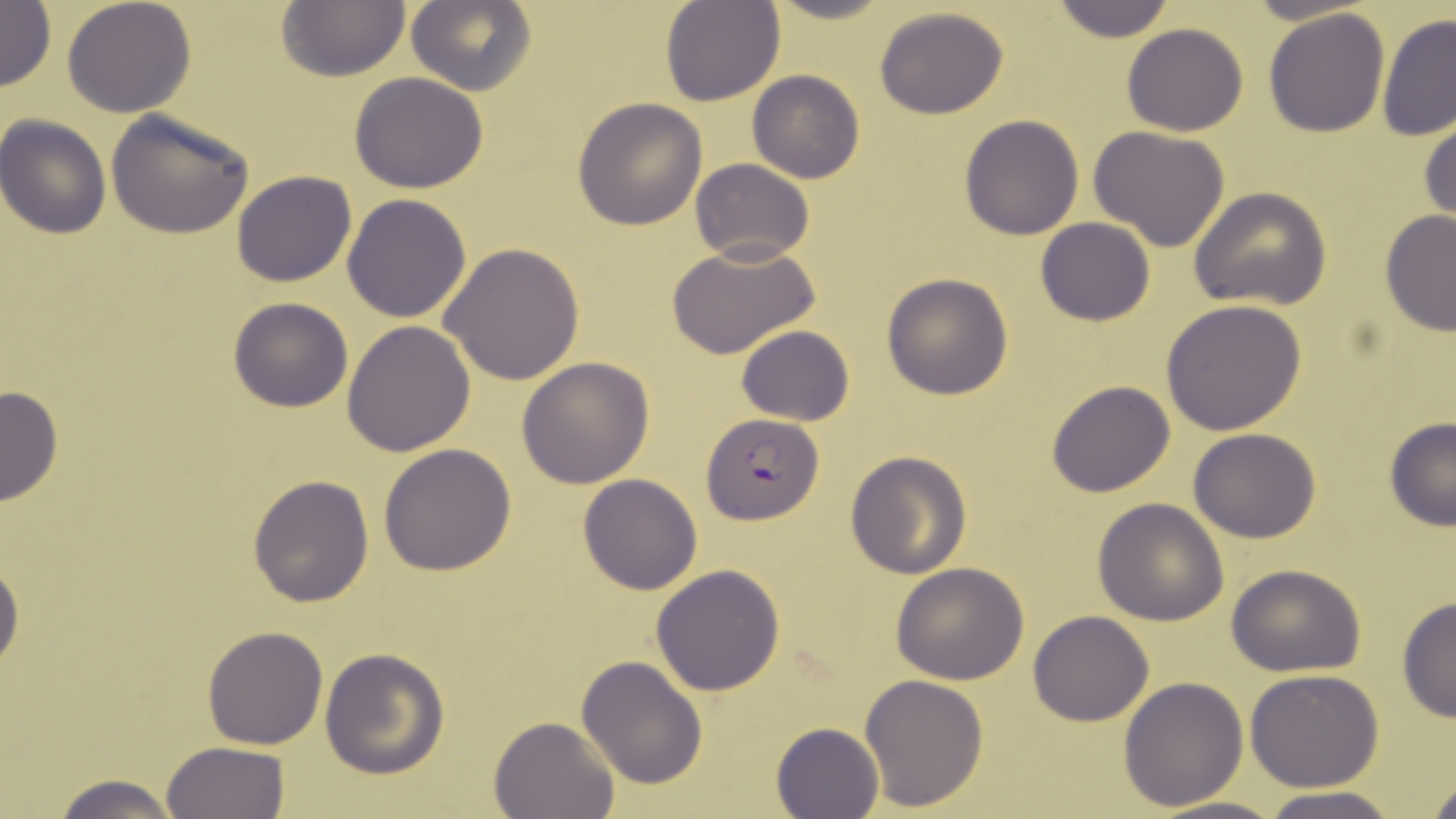
slide-level diagnosis = Plasmodium falciparum
stain = May-Grünwald-Giemsa
preparation = thin blood smear
magnification = 1000x
image size = 1456×819 pixels
uninfected red blood cell locations = approximate bounding boxes as (x1, y1, x2, y2) in pixels: (62, 0, 197, 118), (660, 0, 784, 106), (1047, 0, 1177, 42), (276, 1, 409, 82), (405, 1, 535, 97), (0, 2, 56, 93), (873, 5, 1010, 119), (1263, 8, 1391, 138), (1377, 13, 1455, 141), (1122, 24, 1248, 137), (746, 69, 866, 184), (350, 72, 489, 194), (574, 96, 707, 229), (105, 109, 255, 240), (1417, 109, 1456, 229), (959, 114, 1086, 240), (1, 115, 113, 238), (1087, 126, 1231, 250), (689, 158, 814, 265), (231, 170, 357, 286), (1189, 187, 1333, 312), (341, 193, 473, 323), (1379, 210, 1456, 338), (1035, 217, 1156, 326), (665, 241, 821, 359), (438, 242, 585, 385), (881, 273, 1014, 398), (227, 297, 353, 414), (1163, 300, 1307, 436), (342, 319, 476, 456), (736, 324, 855, 425), (516, 356, 656, 488), (1047, 380, 1176, 498), (0, 383, 63, 507), (1383, 417, 1456, 531), (1189, 427, 1320, 543), (378, 443, 516, 577), (844, 451, 972, 578), (248, 473, 375, 609), (577, 473, 703, 595), (1093, 497, 1229, 626), (0, 552, 23, 680), (890, 563, 1028, 683), (650, 564, 784, 696), (1227, 564, 1367, 676), (1395, 595, 1455, 723), (1028, 609, 1155, 727), (202, 626, 329, 749), (319, 647, 449, 778), (576, 656, 707, 791), (1245, 670, 1386, 792), (859, 674, 989, 812), (1119, 677, 1249, 811), (489, 716, 619, 819), (770, 721, 884, 819), (160, 741, 291, 819), (51, 772, 181, 817), (1425, 774, 1456, 816), (1258, 790, 1400, 819), (1149, 794, 1289, 819)
Plasmodium falciparum-infected red blood cell locations = approximate bounding boxes as (x1, y1, x2, y2) in pixels: (700, 412, 824, 525)
field of view = one of a larger specimen
modality = light microscopy